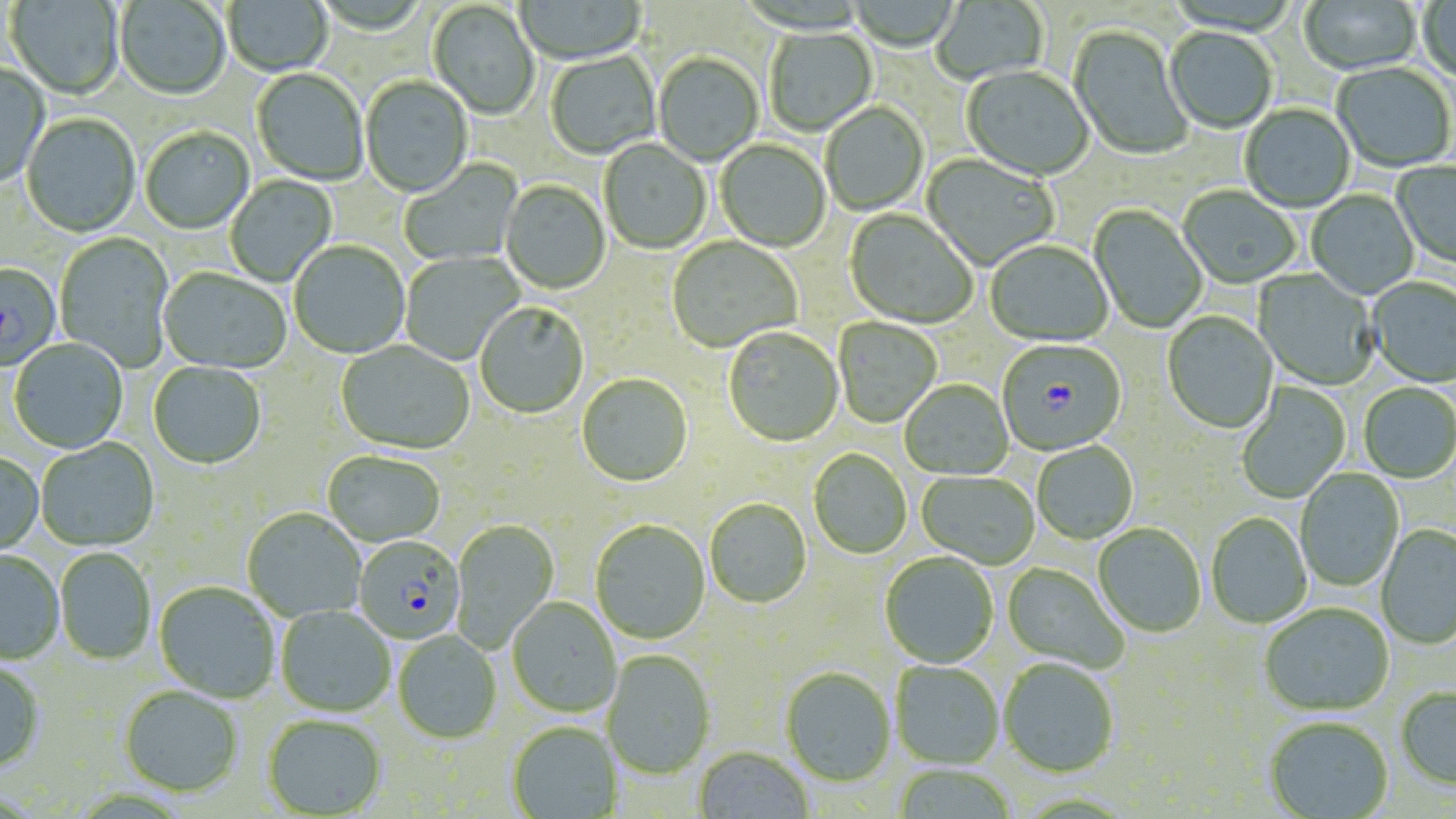

slide_level_diagnosis: Plasmodium falciparum
preparation: thin blood smear
modality: optical microscopy
magnification: 1000x
field_of_view: one of a larger specimen
stain: May-Grünwald-Giemsa
image_size: 1456×819 pixels
uninfected_red_blood_cell_locations: 'approximate bounding boxes as (x1,y1)-(x2,y2) corner pairs in pixels: (7,0)-(124,102), (224,0)-(333,77), (931,0)-(1049,86), (1300,0)-(1422,77), (1417,0)-(1455,85), (115,1)-(230,102), (515,1)-(646,66), (428,2)-(539,121), (1067,25)-(1194,161), (764,28)-(878,137), (1165,28)-(1277,135), (546,51)-(661,160), (653,54)-(763,167), (0,63)-(50,189), (1332,63)-(1455,173), (961,67)-(1093,183), (252,69)-(368,187), (360,77)-(473,199), (821,102)-(929,216), (1240,104)-(1355,213), (22,115)-(140,238), (140,128)-(254,235), (599,140)-(711,255), (715,140)-(830,253), (921,154)-(1058,271), (400,159)-(523,267), (1392,160)-(1456,270), (226,175)-(337,287), (501,181)-(610,295), (1178,187)-(1300,290), (1307,190)-(1418,300), (1089,205)-(1207,333), (844,209)-(977,330), (55,232)-(174,371), (667,237)-(801,353), (290,241)-(410,359), (985,241)-(1113,347), (400,251)-(524,364), (0,263)-(61,371), (158,269)-(290,376), (1254,269)-(1379,390), (1367,278)-(1456,388), (475,304)-(589,419), (1162,312)-(1279,435), (833,318)-(941,428), (724,329)-(843,448), (9,339)-(128,455), (336,341)-(474,456), (148,363)-(266,471), (576,375)-(693,488), (900,380)-(1013,481), (1236,382)-(1350,503), (1358,383)-(1456,484), (36,439)-(159,552), (1032,441)-(1139,545), (809,449)-(912,560), (0,452)-(44,557), (323,452)-(445,548), (1295,469)-(1405,591), (916,472)-(1039,570), (705,499)-(811,610), (242,510)-(366,623), (1206,513)-(1312,629), (451,520)-(559,651), (590,520)-(710,646), (1093,525)-(1206,638), (1376,525)-(1456,650), (55,548)-(156,665), (0,551)-(64,664), (880,553)-(998,669), (1002,563)-(1129,673), (154,582)-(279,704), (507,599)-(621,718), (1259,604)-(1394,718), (276,607)-(395,717), (393,632)-(502,745), (602,651)-(716,780), (999,658)-(1119,778), (890,661)-(1004,770), (0,662)-(46,773), (780,668)-(895,788), (119,687)-(243,799), (1396,688)-(1456,792), (262,717)-(386,818), (1265,719)-(1393,818), (507,723)-(621,818), (694,748)-(813,819), (892,764)-(1018,819)'
plasmodium_falciparum_infected_red_blood_cell_locations: 'approximate bounding boxes as (x1,y1)-(x2,y2) corner pairs in pixels: (997,340)-(1126,457), (355,536)-(461,640)'